Describe the morphology of the erythrocytes.
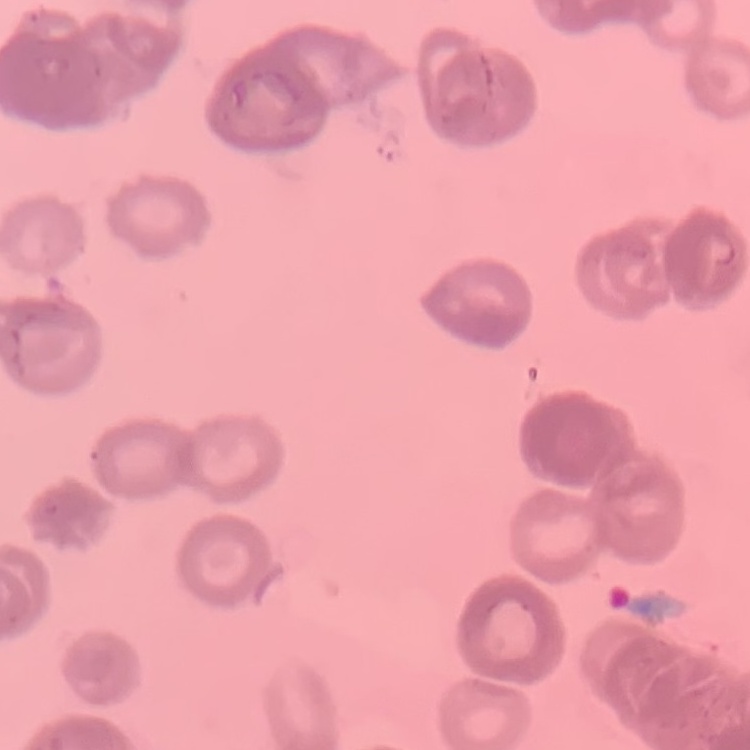
They show rouleaux formation.

Stained with either Field's or Giemsa. One tile cut from a larger photomicrograph. Thin peripheral smear.